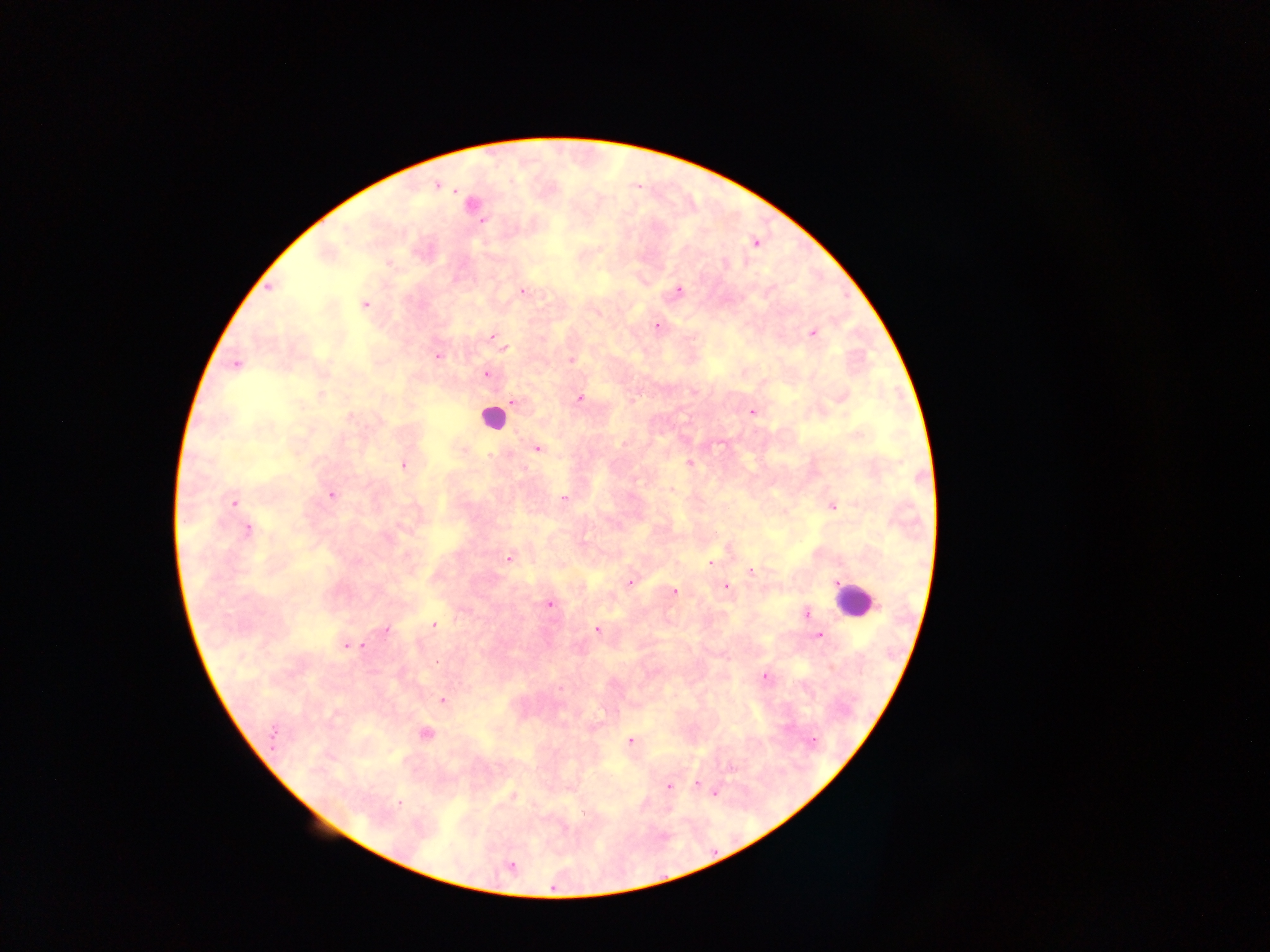
Approximate centers as [x, y] in pixels.
Summary:
  - Leukocyte locations: [492, 416], [857, 602]
  - Malaria parasite locations: [436, 186], [455, 192], [479, 218], [385, 263], [676, 289], [520, 291], [366, 304], [654, 326], [814, 333], [489, 337], [504, 349], [438, 356], [569, 360], [235, 362], [485, 374], [579, 397], [513, 401], [751, 410], [460, 449], [536, 449], [689, 463], [403, 466], [331, 495], [564, 498], [233, 501], [833, 506], [249, 529], [510, 558], [710, 562], [751, 571], [630, 580], [724, 586], [675, 591], [548, 603], [804, 613], [434, 625], [597, 630], [386, 631], [819, 636], [343, 645], [359, 647], [438, 661], [765, 678], [442, 701], [274, 733], [425, 734], [629, 740], [271, 751], [730, 768], [699, 783], [669, 787], [718, 791], [398, 803], [583, 812]
  - Image size: 1270×952 pixels
  - Preparation: thick blood film
  - Field of view: single
  - Country: Ghana
  - Capture: mobile-phone photograph through a microscope